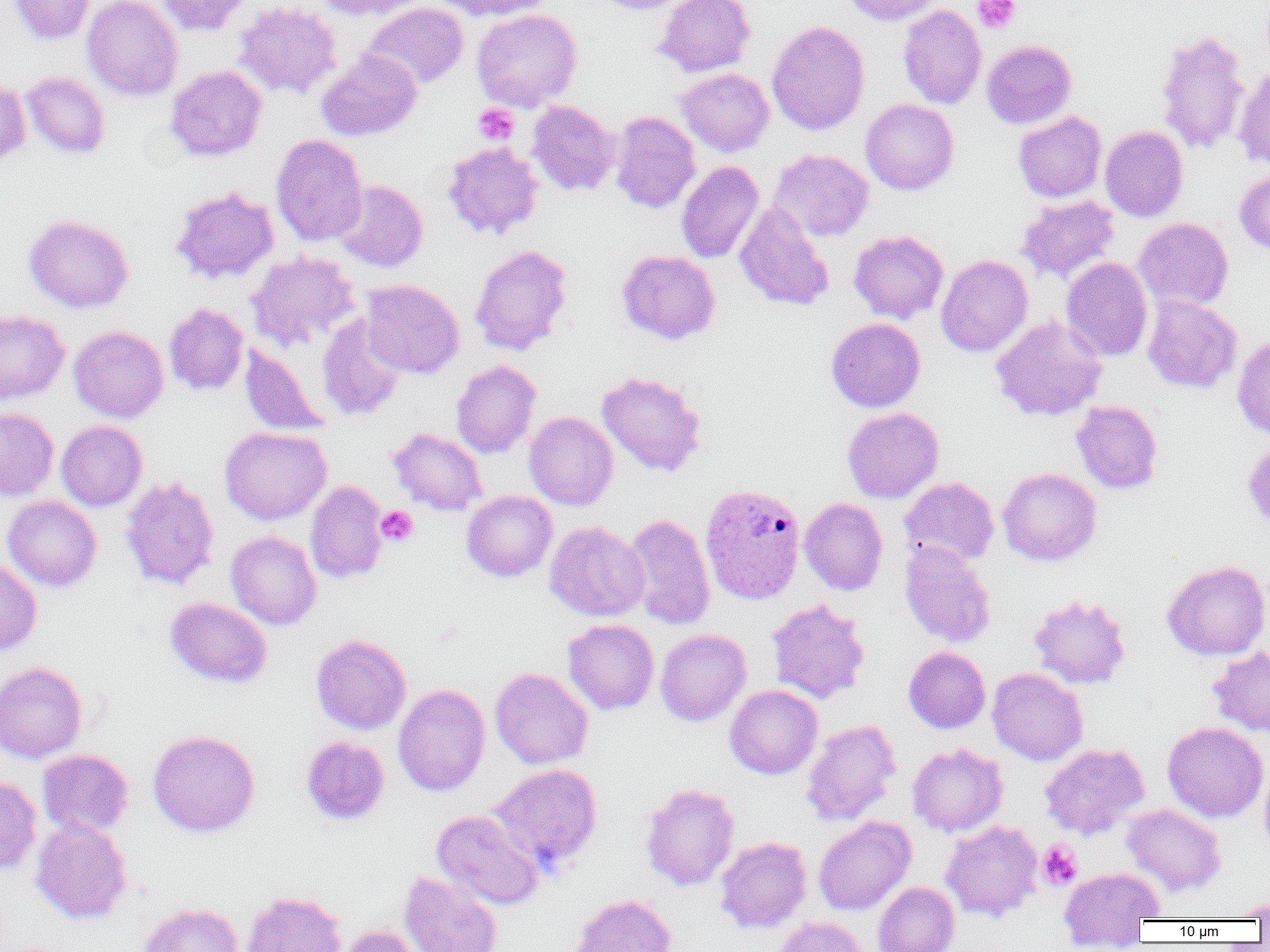

Approximate bounding boxes as (x1, y1, x2, y2) in pixels. Plasmodium vivax-infected red blood cell locations: (700, 483, 806, 604). Platelet locations: (972, 0, 1020, 34), (473, 103, 519, 146), (375, 505, 418, 547), (1038, 840, 1082, 889). Uninfected red blood cell locations: (9, 0, 95, 45), (83, 0, 183, 101), (155, 0, 252, 36), (311, 0, 428, 20), (434, 0, 555, 21), (590, 0, 695, 15), (654, 0, 755, 78), (842, 0, 944, 26), (233, 1, 343, 100), (361, 3, 469, 89), (360, 4, 582, 95), (898, 5, 986, 109), (471, 9, 582, 112), (767, 20, 870, 136), (1154, 28, 1250, 156), (981, 40, 1077, 129), (316, 49, 422, 141), (1234, 64, 1270, 172), (165, 65, 267, 161), (675, 68, 774, 157), (21, 71, 110, 159), (0, 79, 31, 166), (860, 99, 959, 195), (527, 100, 620, 196), (609, 111, 700, 214), (1013, 111, 1107, 202), (1100, 126, 1188, 221), (271, 134, 368, 246), (442, 141, 544, 240), (769, 149, 874, 242), (676, 160, 764, 264), (1234, 168, 1270, 256), (332, 180, 428, 272), (170, 186, 279, 284), (1016, 194, 1120, 285), (734, 202, 834, 312), (24, 214, 134, 313), (1134, 217, 1234, 311), (848, 230, 949, 324), (470, 244, 572, 356), (617, 250, 721, 344), (246, 251, 360, 352), (935, 255, 1033, 357), (1061, 257, 1152, 362), (360, 279, 464, 379), (1142, 295, 1242, 393), (164, 302, 249, 396), (0, 310, 69, 405), (317, 314, 407, 421), (990, 315, 1107, 421), (826, 317, 926, 412), (69, 326, 169, 423), (1232, 333, 1270, 440), (240, 343, 329, 436), (451, 360, 541, 458), (596, 371, 707, 477), (1071, 400, 1163, 494), (0, 407, 58, 500), (842, 407, 944, 503), (524, 412, 618, 510), (56, 420, 147, 511), (219, 426, 331, 525), (388, 427, 488, 516), (1242, 439, 1270, 531), (997, 468, 1102, 566), (119, 476, 220, 591), (898, 476, 999, 568), (305, 480, 388, 583), (461, 491, 558, 582), (2, 496, 102, 591), (799, 498, 888, 596), (623, 513, 715, 631), (545, 521, 649, 622), (225, 531, 322, 630), (899, 542, 996, 648), (0, 557, 42, 657), (1162, 560, 1270, 660), (1028, 594, 1131, 690), (165, 597, 273, 688), (766, 599, 870, 704), (563, 619, 659, 714), (655, 628, 751, 726), (311, 633, 411, 735), (903, 646, 990, 734), (1208, 646, 1270, 737), (0, 661, 88, 763), (489, 667, 593, 769), (987, 667, 1088, 766), (393, 684, 490, 796), (724, 685, 823, 779), (801, 719, 902, 826), (1162, 722, 1268, 822), (147, 729, 260, 837), (300, 736, 390, 825), (907, 743, 1008, 837), (1039, 743, 1149, 840), (37, 749, 134, 839), (1259, 759, 1270, 863), (487, 763, 602, 873), (0, 774, 42, 876), (639, 783, 740, 890), (1121, 803, 1226, 896), (431, 809, 544, 909), (814, 816, 916, 915), (31, 818, 132, 923), (940, 820, 1043, 922), (715, 836, 812, 933), (1058, 867, 1165, 945), (399, 871, 503, 952), (872, 881, 960, 952), (242, 891, 346, 952), (570, 894, 677, 952), (1231, 897, 1270, 920), (138, 902, 244, 952), (773, 916, 868, 952), (338, 925, 427, 952). Slide-level diagnosis: Plasmodium vivax. Image is 1270×952 pixels. 1000x magnification. Single field of view. Thin blood film. Light microscopy.